Classify this cell by malaria status.
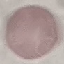
Uninfected.

Summary:
  - Stain: Giemsa
  - Preparation: thin blood smear
  - Capture: smartphone camera at the microscope eyepiece
  - Image type: automatically extracted cell patch, resized to 64 × 64 pixels